Name the parasite shown.
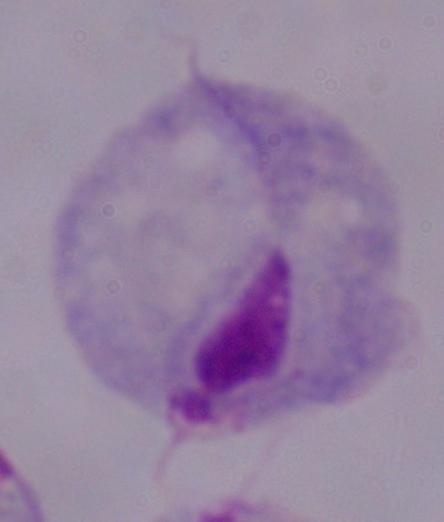
This is a trichomonad.

magnification = 1000x
modality = photomicrograph